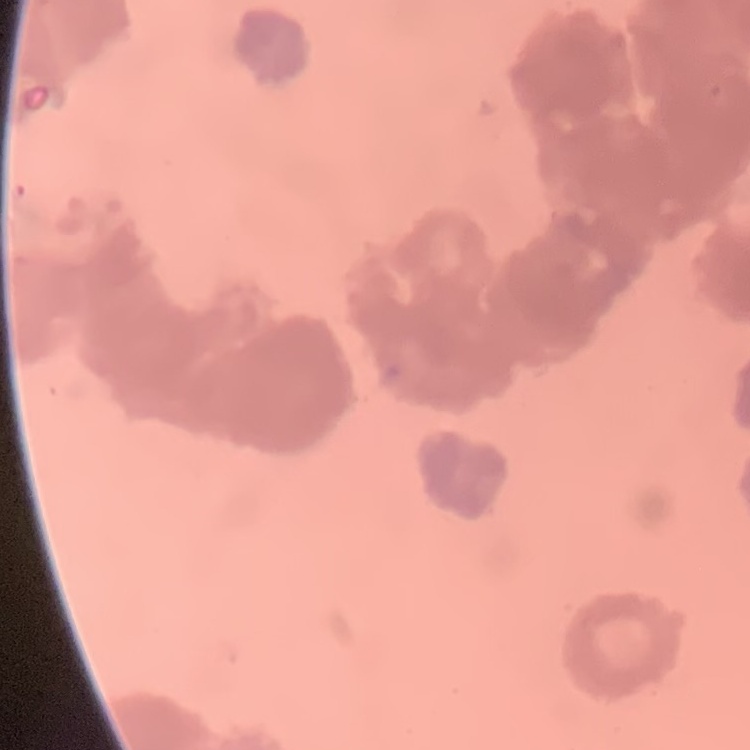

erythrocyte morphology = rouleaux formation
preparation = thin blood smear
stain = Field's or Giemsa
image type = one tile cut from a larger photomicrograph